Report the malaria status of this cell.
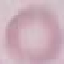

Uninfected.

Summary:
  - Image type: automatically extracted cell patch, resized to 64 × 64 pixels
  - Preparation: thin blood smear
  - Stain: Giemsa
  - Capture: smartphone camera at the microscope eyepiece